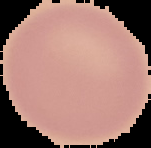
image size = 151×148 pixels
image type = segmented cell region with the area outside set to black
malaria status = uninfected
preparation = thin blood film